Give the extent of all uninfected red blood cells.
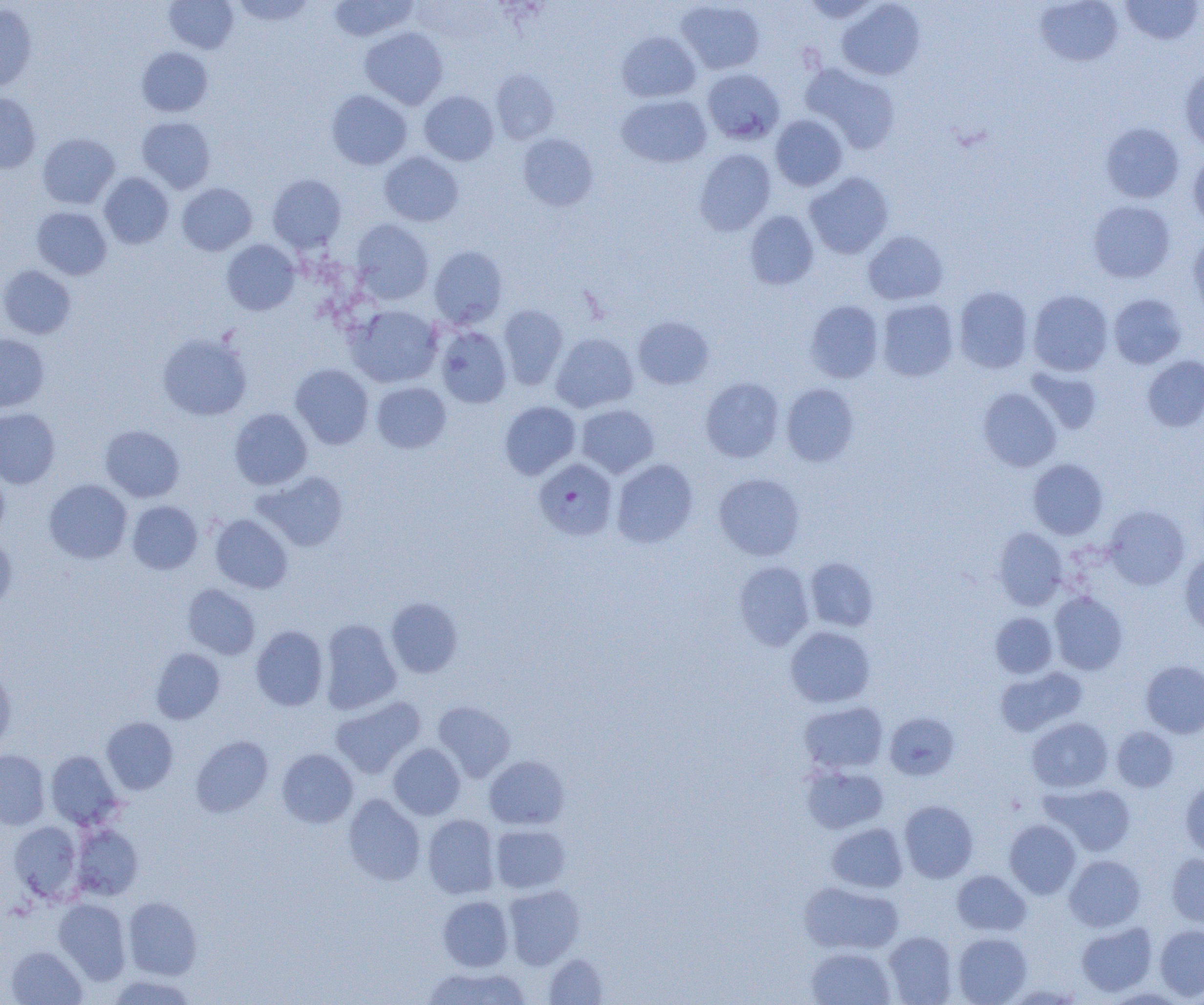

Approximate bounding boxes as (x1, y1, x2, y2) in pixels.
Uninfected red blood cells: (231, 0, 317, 26), (800, 0, 881, 23), (1034, 0, 1123, 66), (1120, 0, 1203, 45), (164, 1, 238, 54), (327, 1, 418, 42), (676, 1, 765, 74), (836, 1, 925, 80), (0, 2, 37, 91), (360, 27, 448, 109), (617, 31, 701, 102), (137, 47, 213, 117), (801, 63, 901, 154), (1180, 67, 1204, 151), (703, 68, 785, 144), (491, 69, 560, 145), (326, 90, 412, 170), (419, 90, 498, 165), (0, 93, 41, 173), (616, 94, 712, 168), (770, 115, 848, 191), (137, 116, 215, 192), (1100, 122, 1184, 203), (37, 133, 119, 209), (518, 133, 598, 211), (693, 149, 776, 236), (1188, 151, 1204, 230), (379, 152, 463, 226), (804, 171, 894, 258), (99, 173, 174, 248), (267, 174, 347, 252), (176, 183, 257, 255), (1088, 200, 1175, 283), (32, 207, 112, 279), (744, 210, 819, 290), (351, 219, 433, 304), (863, 230, 948, 305), (1188, 233, 1204, 321), (221, 239, 300, 315), (429, 246, 508, 329), (0, 265, 76, 339), (953, 286, 1033, 374), (1028, 290, 1114, 376), (1108, 293, 1187, 368), (876, 299, 959, 381), (805, 300, 884, 383), (498, 304, 568, 389), (346, 305, 443, 388), (633, 316, 714, 389), (436, 326, 512, 408), (157, 332, 252, 421), (551, 332, 638, 413), (0, 334, 49, 413), (1142, 355, 1204, 431), (290, 364, 374, 449), (1026, 366, 1103, 434), (701, 377, 784, 462), (371, 382, 451, 453), (781, 383, 859, 466), (978, 387, 1061, 472), (499, 401, 581, 479), (576, 404, 659, 478), (0, 407, 60, 488), (229, 408, 312, 490), (100, 424, 184, 502), (612, 459, 698, 548), (1028, 459, 1108, 539), (0, 471, 9, 540), (253, 471, 348, 552), (713, 473, 805, 560), (44, 479, 132, 563), (127, 501, 202, 574), (1104, 506, 1189, 590), (210, 513, 293, 593), (993, 527, 1068, 610), (0, 535, 16, 613), (1179, 551, 1204, 637), (805, 557, 879, 632), (733, 560, 815, 651), (182, 584, 260, 659), (1049, 591, 1128, 675), (386, 597, 463, 678), (990, 612, 1057, 678), (320, 619, 402, 714), (251, 625, 328, 711), (785, 626, 876, 708), (151, 648, 225, 724), (1141, 660, 1204, 738), (0, 665, 16, 751), (996, 666, 1087, 737), (331, 696, 425, 778), (432, 701, 515, 782), (799, 701, 888, 773), (884, 711, 960, 780), (101, 717, 178, 794), (1027, 717, 1113, 793), (1112, 726, 1179, 792), (191, 735, 273, 817), (388, 742, 465, 819), (277, 748, 358, 828), (0, 750, 50, 830), (46, 750, 123, 830), (484, 755, 569, 830), (801, 764, 889, 833), (1180, 779, 1204, 858), (1044, 784, 1136, 856), (344, 794, 426, 886), (899, 800, 978, 882), (423, 814, 500, 899), (1004, 819, 1081, 898), (8, 821, 82, 902), (826, 822, 908, 893), (71, 824, 143, 900), (490, 824, 570, 893), (1167, 853, 1204, 929), (1065, 855, 1145, 931), (952, 870, 1031, 936), (799, 881, 904, 955), (504, 884, 585, 969), (438, 895, 513, 971), (123, 896, 202, 980), (53, 899, 131, 984), (1076, 923, 1157, 996), (1155, 924, 1204, 1001), (883, 931, 957, 1004), (953, 932, 1032, 1004), (6, 946, 87, 1005), (806, 946, 895, 1005), (543, 953, 608, 1004), (421, 966, 532, 1005), (106, 974, 198, 1005), (1005, 984, 1084, 1004), (1103, 988, 1188, 1004).

Plasmodium falciparum-infected red blood cell locations: (533, 458, 617, 540). Slide-level diagnosis: Plasmodium falciparum. Thin blood smear. Light microscopy. Image is 1204×1005 pixels. Captured at 1000x magnification. Single field of view.